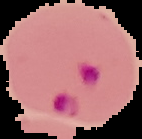
Summary:
  - Preparation: thin blood film
  - Result: Plasmodium parasites detected
  - Image type: segmented cell region with the area outside set to black
  - Image size: 142×139 pixels